Describe the morphology of the red blood cells.
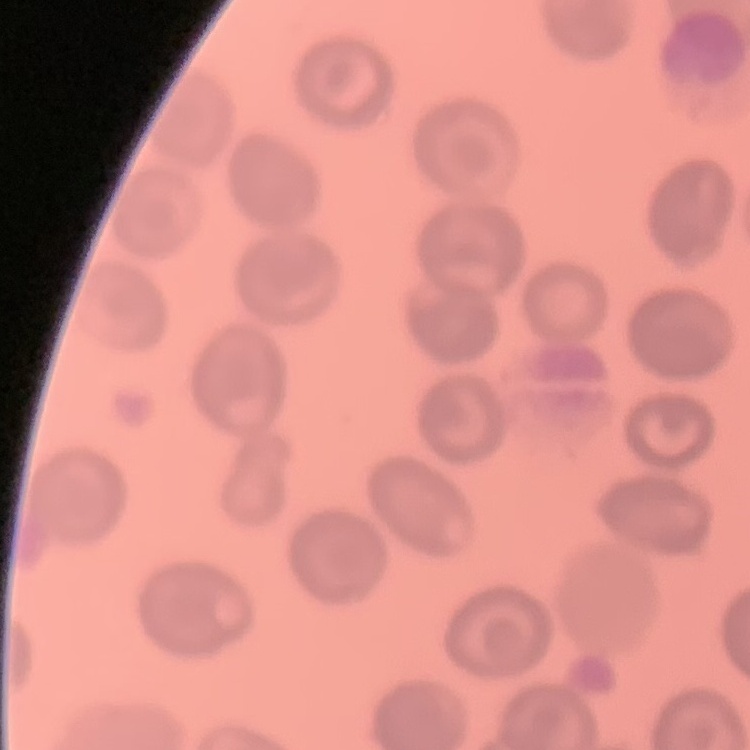
They show no rouleaux formation.

Summary:
  - Stain: Field's or Giemsa
  - Preparation: thin blood smear
  - Image type: square crop of a larger photomicrograph